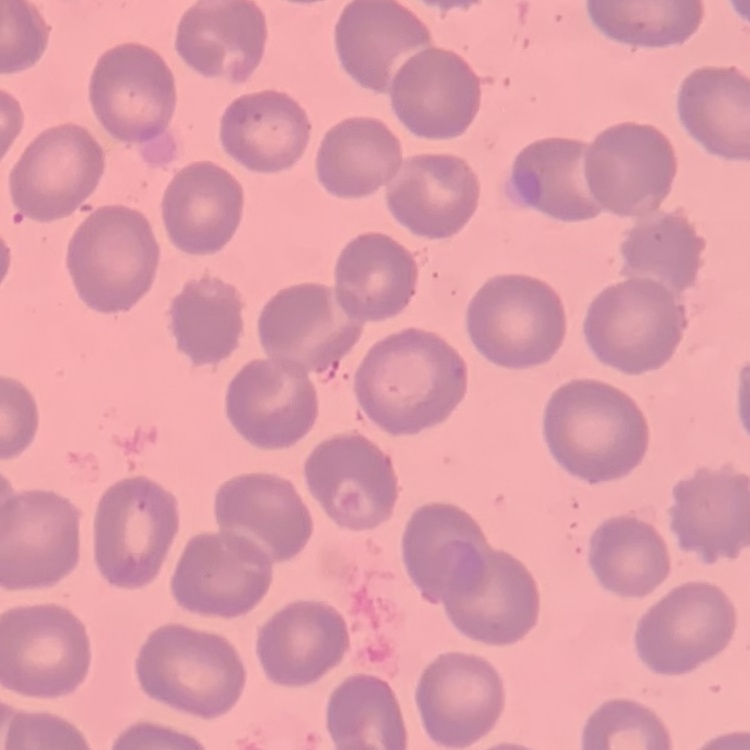
Summary:
  - Erythrocyte morphology: no rouleaux formation
  - Preparation: thin blood film
  - Image type: one tile cut from a larger photomicrograph
  - Stain: Field's or Giemsa